Describe the morphology of the erythrocytes.
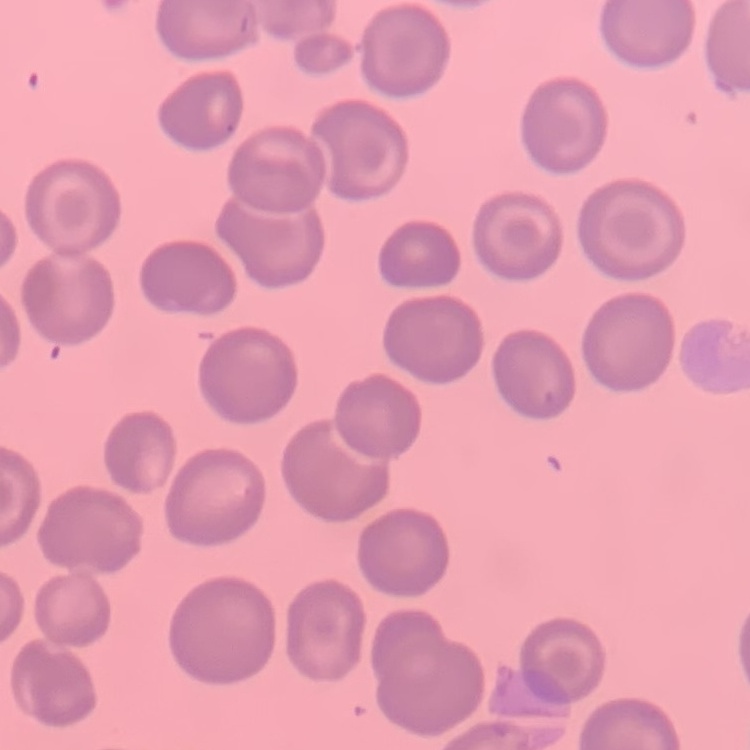
No rouleaux formation.

Stained with either Field's or Giemsa. Thin blood smear. One tile cut from a larger photomicrograph.